Report the malaria status of this cell.
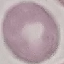
It is uninfected.

Cell patch, automatically extracted from a larger field of view and resized to 64 × 64 pixels. Giemsa stain. Thin blood film. Photographed with a smartphone camera at the microscope eyepiece.